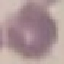
Malaria status: uninfected. Thin blood smear. Automatically extracted cell patch, resized to 64 × 64 pixels. Acquired by smartphone through the microscope eyepiece. Giemsa-stained preparation.